Report the malaria status of this cell.
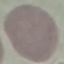
It is uninfected.

Acquired by smartphone through the microscope eyepiece. Cell patch, automatically extracted from a larger field of view and resized to 64 × 64 pixels. Thin blood film. Giemsa stain.